Locate malaria parasites and leukocytes.
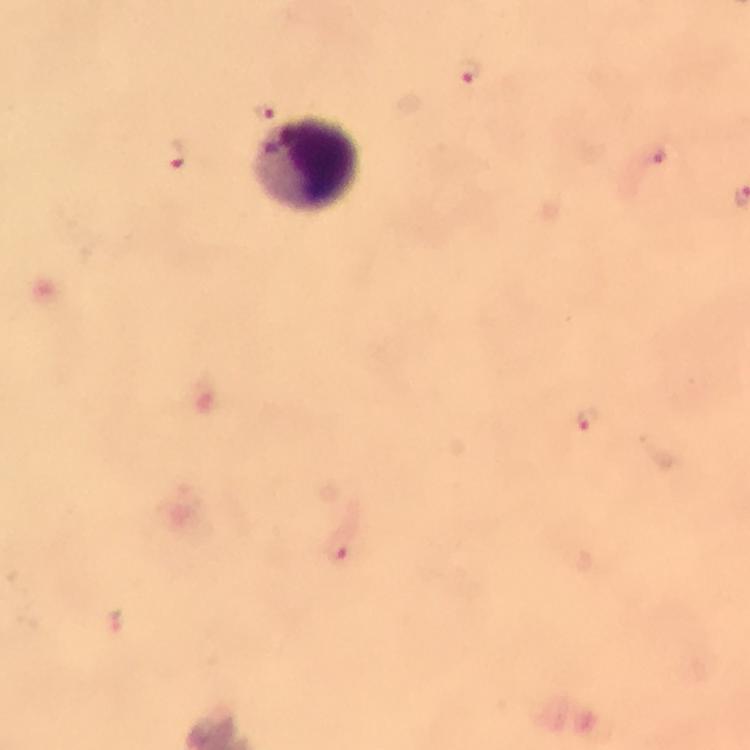
Approximate centers as [x, y] in pixels.
Malaria parasites: [466, 69], [260, 109], [177, 153], [653, 155], [585, 418], [339, 551], [116, 621].
Leukocytes: [307, 164].

preparation = thick smear
immersion oil = used
capture = smartphone photograph through a microscope
cropped from = a single field of view
image size = 750×750 pixels
magnification = 100x
context = from a diagnostic examination for malaria
stain = Giemsa